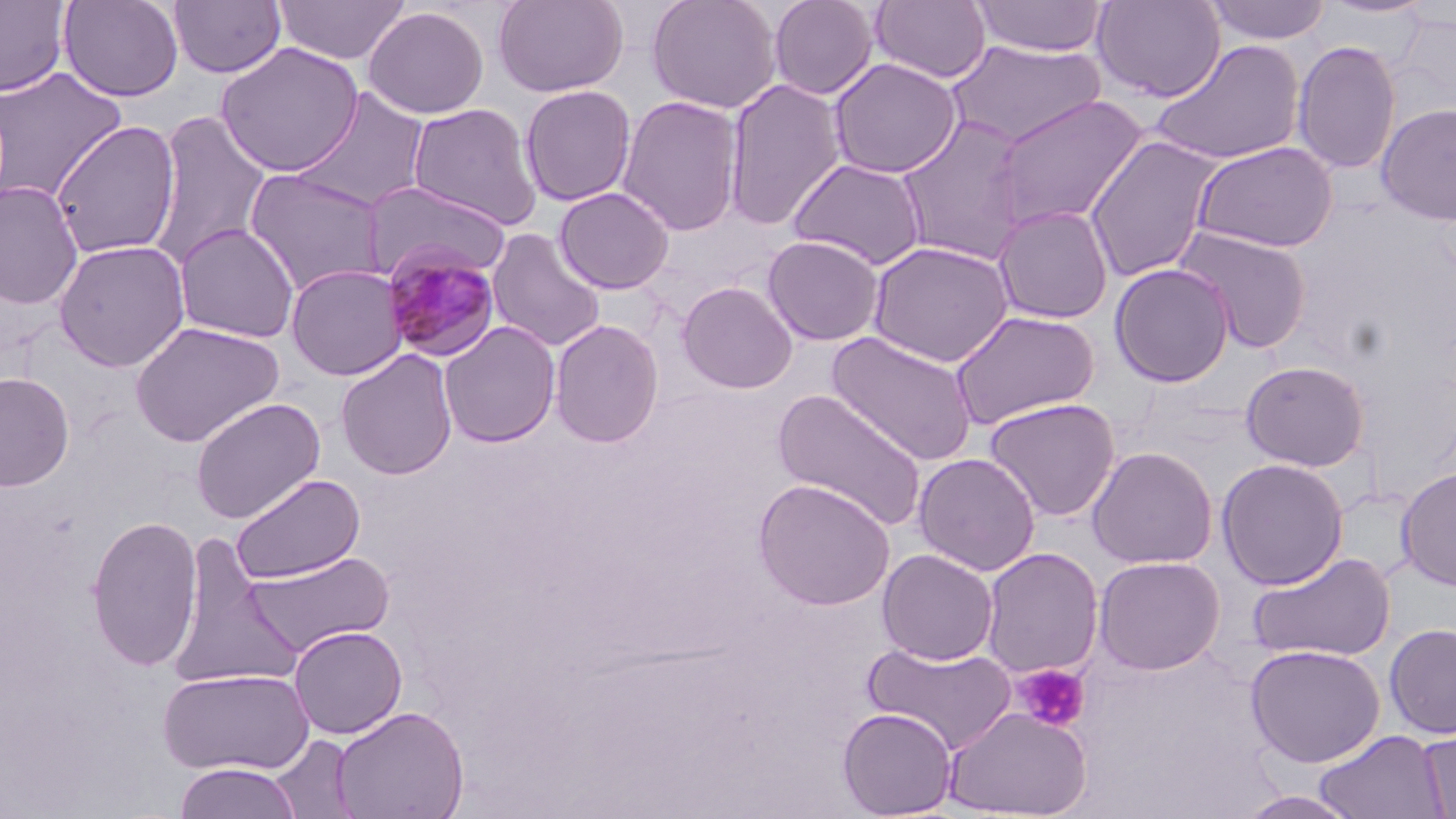 Approximate bounding boxes as (x1,y1)-(x2,y2) corner pairs in pixels. Uninfected red blood cell locations: (58,0)-(183,102), (167,0)-(287,79), (273,0)-(410,65), (492,0)-(628,98), (647,0)-(781,114), (768,0)-(878,100), (871,0)-(991,84), (970,0)-(1109,57), (1092,0)-(1226,103), (0,1)-(71,97), (1202,1)-(1333,45), (363,6)-(489,119), (1391,11)-(1456,115), (1148,39)-(1306,165), (945,40)-(1106,148), (1292,40)-(1401,176), (215,42)-(363,177), (828,57)-(962,179), (0,66)-(127,205), (724,78)-(847,231), (520,84)-(636,207), (293,87)-(430,213), (988,93)-(1151,232), (616,95)-(744,237), (1375,102)-(1456,225), (407,103)-(543,231), (148,111)-(271,270), (896,115)-(1031,264), (50,120)-(181,259), (1084,135)-(1224,282), (1191,140)-(1340,253), (787,157)-(928,271), (244,168)-(388,295), (362,179)-(508,282), (0,180)-(84,310), (554,187)-(674,294), (992,204)-(1114,324), (174,222)-(300,343), (1173,224)-(1313,354), (486,228)-(607,353), (762,235)-(885,346), (53,239)-(190,372), (867,240)-(1014,368), (1109,262)-(1236,387), (285,264)-(408,381), (677,281)-(798,393), (948,310)-(1101,430), (549,319)-(664,449), (129,320)-(285,448), (439,321)-(561,448), (826,331)-(979,466), (335,349)-(458,481), (1239,360)-(1372,471), (0,371)-(75,491), (772,388)-(928,532), (189,397)-(326,524), (983,397)-(1121,522), (1086,445)-(1219,569), (913,452)-(1041,576), (1216,458)-(1349,589), (1396,466)-(1456,592), (230,473)-(365,585), (753,479)-(895,611), (85,513)-(204,672), (168,540)-(303,691), (980,547)-(1104,679), (877,548)-(999,666), (244,551)-(395,656), (1246,551)-(1397,663), (1093,554)-(1226,675), (1384,623)-(1456,739), (288,624)-(408,739), (861,640)-(1018,754), (1244,642)-(1386,767), (158,668)-(315,776), (942,705)-(1092,819), (330,706)-(468,819), (837,707)-(958,818), (1417,728)-(1456,818), (1312,729)-(1448,819), (268,734)-(360,818), (173,762)-(304,819), (1235,790)-(1364,818). Plasmodium malariae-infected red blood cell locations: (380,243)-(503,364). Platelet locations: (1014,663)-(1090,732). Slide-level diagnosis: Plasmodium malariae. Image is 1456×819 pixels. Optical microscopy. May-Grünwald-Giemsa-stained preparation. Captured at 1000x magnification. Thin blood film. One field of a larger specimen.